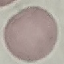
malaria status = uninfected
stain = Giemsa
capture = smartphone through the microscope eyepiece
image type = cell patch, automatically extracted from a larger field of view and resized to 64 × 64 pixels
preparation = thin smear